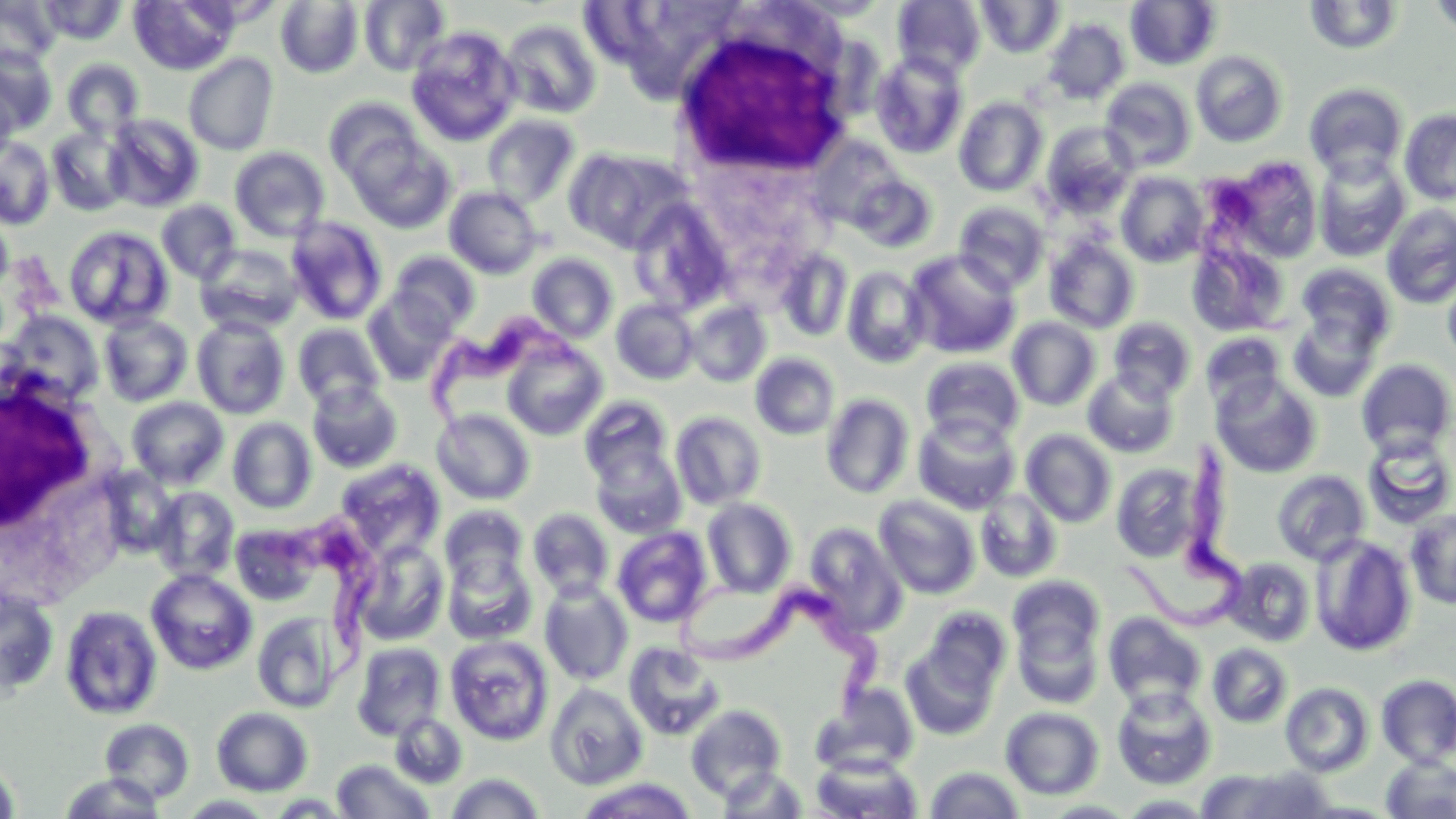
slide-level diagnosis = Trypanosoma brucei
white blood cell locations = approximate bounding boxes as (x1, y1, x2, y2) in pixels: (672, 23, 854, 178), (0, 379, 112, 546)
field of view = one of a larger specimen
modality = optical microscopy
image size = 1456×819 pixels
Trypanosoma brucei locations = approximate bounding boxes as (x1, y1, x2, y2) in pixels: (1204, 155, 1314, 347), (428, 310, 587, 455), (1123, 443, 1252, 632), (272, 519, 378, 682), (673, 565, 896, 723)
stain = May-Grünwald-Giemsa
preparation = thin blood smear
magnification = 1000x
uninfected red blood cell locations = approximate bounding boxes as (x1, y1, x2, y2) in pixels: (38, 0, 126, 44), (129, 0, 238, 75), (359, 0, 450, 76), (892, 0, 986, 80), (976, 0, 1065, 58), (1428, 0, 1456, 39), (0, 1, 59, 69), (275, 1, 364, 78), (1126, 1, 1222, 70), (1304, 1, 1404, 55), (1043, 18, 1130, 104), (500, 19, 602, 119), (406, 26, 522, 146), (1, 46, 56, 132), (1191, 50, 1288, 147), (871, 52, 968, 159), (183, 54, 278, 155), (62, 59, 144, 139), (1100, 78, 1197, 171), (0, 79, 19, 167), (1304, 83, 1409, 182), (324, 97, 423, 182), (954, 97, 1049, 197), (1399, 109, 1456, 205), (104, 114, 204, 212), (482, 115, 581, 208), (1040, 123, 1138, 219), (47, 127, 131, 216), (0, 136, 56, 229), (349, 136, 454, 234), (230, 147, 330, 241), (564, 147, 679, 252), (1221, 156, 1324, 261), (1313, 156, 1410, 262), (1116, 172, 1209, 267), (848, 173, 938, 253), (444, 187, 543, 278), (156, 200, 241, 284), (953, 201, 1049, 294), (630, 202, 734, 316), (1381, 204, 1456, 309), (0, 211, 14, 299), (286, 217, 388, 326), (63, 225, 174, 331), (1044, 237, 1140, 333), (1187, 241, 1289, 336), (197, 244, 303, 333), (776, 249, 852, 342), (905, 250, 1020, 359), (389, 251, 480, 334), (527, 253, 618, 343), (1296, 263, 1396, 354), (1441, 265, 1456, 365), (841, 266, 931, 368), (364, 291, 456, 385), (611, 299, 699, 385), (685, 300, 772, 387), (2, 310, 104, 406), (99, 313, 193, 406), (1288, 314, 1381, 402), (192, 316, 290, 419), (1007, 317, 1101, 411), (1108, 317, 1196, 402), (293, 322, 386, 410), (1201, 332, 1286, 409), (502, 341, 608, 441), (750, 352, 840, 440), (920, 356, 1024, 446), (1356, 359, 1456, 458), (1082, 369, 1179, 458), (1211, 374, 1322, 478), (307, 381, 403, 473), (821, 394, 915, 499), (579, 396, 674, 488), (127, 397, 229, 489), (432, 408, 534, 505), (670, 411, 767, 509), (913, 415, 1020, 514), (227, 417, 317, 515), (1021, 429, 1117, 528), (1361, 435, 1456, 530), (590, 445, 686, 538), (336, 459, 444, 558), (1111, 463, 1208, 563), (1272, 469, 1370, 566), (151, 486, 239, 582), (975, 489, 1062, 582), (874, 495, 981, 599), (702, 497, 798, 598), (439, 505, 529, 592), (1405, 507, 1456, 609), (528, 508, 615, 601), (230, 522, 321, 605), (804, 523, 906, 634), (612, 526, 713, 628), (1311, 535, 1417, 656), (354, 539, 450, 645), (442, 551, 537, 645), (1223, 556, 1316, 646), (146, 568, 257, 675), (1008, 575, 1105, 664), (539, 580, 633, 686), (0, 585, 60, 699), (59, 604, 163, 720), (924, 607, 1012, 691), (252, 610, 345, 713), (1104, 612, 1207, 711), (1012, 615, 1104, 708), (444, 635, 554, 746), (901, 640, 1000, 740), (352, 642, 446, 740), (624, 642, 725, 741), (1206, 643, 1293, 728), (1376, 674, 1456, 768), (545, 682, 648, 790), (1280, 682, 1374, 777), (811, 685, 918, 778), (1111, 686, 1217, 790), (685, 704, 787, 800), (212, 707, 313, 796), (1000, 707, 1104, 800), (389, 712, 468, 787), (99, 718, 195, 804), (810, 754, 923, 818), (1381, 755, 1456, 818), (0, 758, 20, 819), (331, 759, 435, 818), (715, 766, 809, 817), (924, 766, 1024, 819), (1197, 766, 1334, 818), (58, 772, 167, 818), (445, 772, 547, 818), (575, 777, 698, 818), (177, 794, 279, 818), (1117, 794, 1218, 817), (1039, 800, 1142, 818)